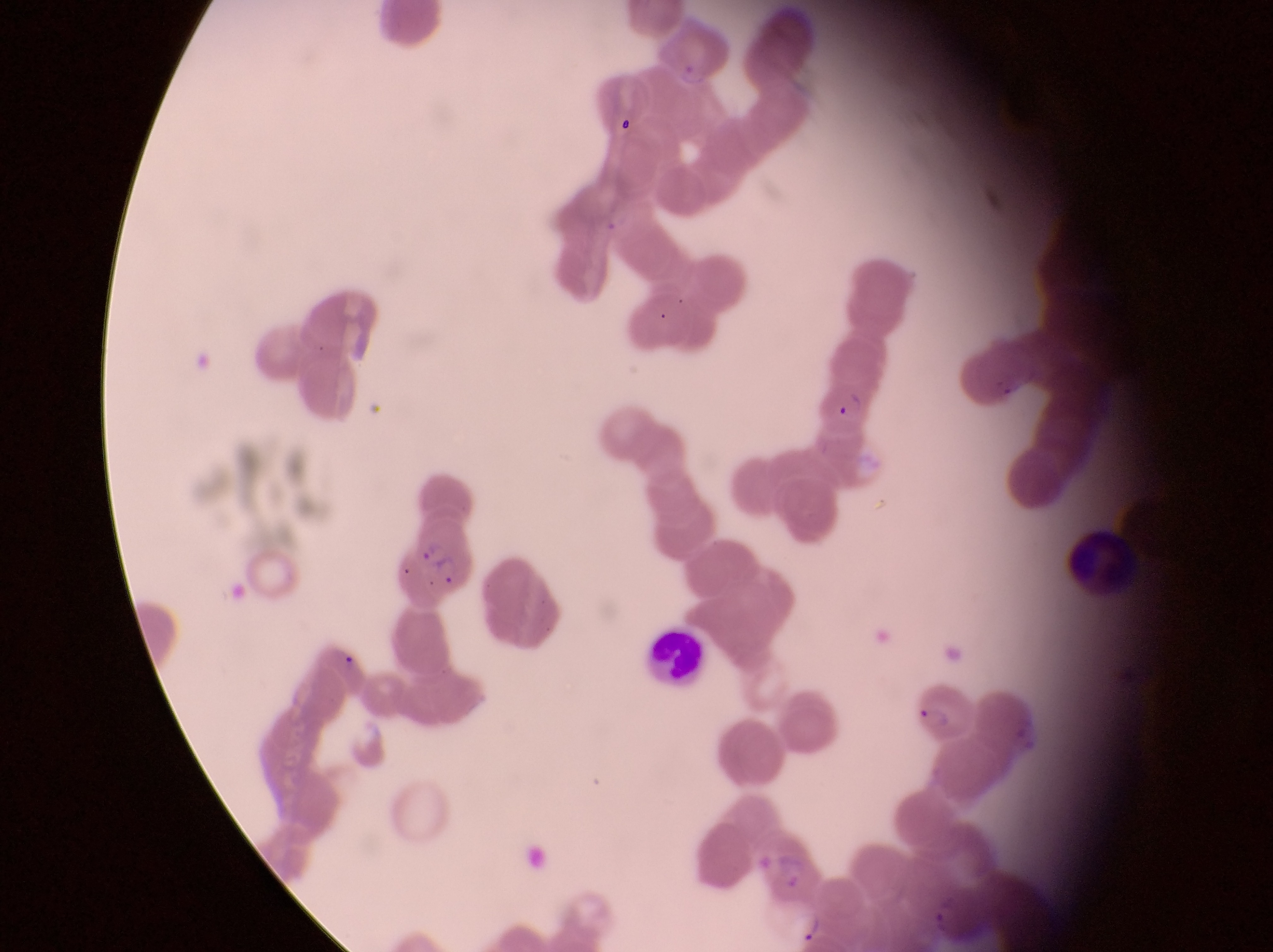
Approximate bounding boxes as (left, top, right, bottom) in pixels. Trophozoite locations: (787, 907, 824, 944). Leukocyte locations: (1073, 525, 1140, 599), (650, 627, 708, 696). Parasitised red blood cell locations: (387, 522, 477, 609), (908, 672, 973, 742). Captured by a smartphone held over the eyepiece of an Olympus CX-23 microscope. Image is 1273×952 pixels. One field of view. Magnification of 1000x. Sample from Uganda. Thin blood smear.